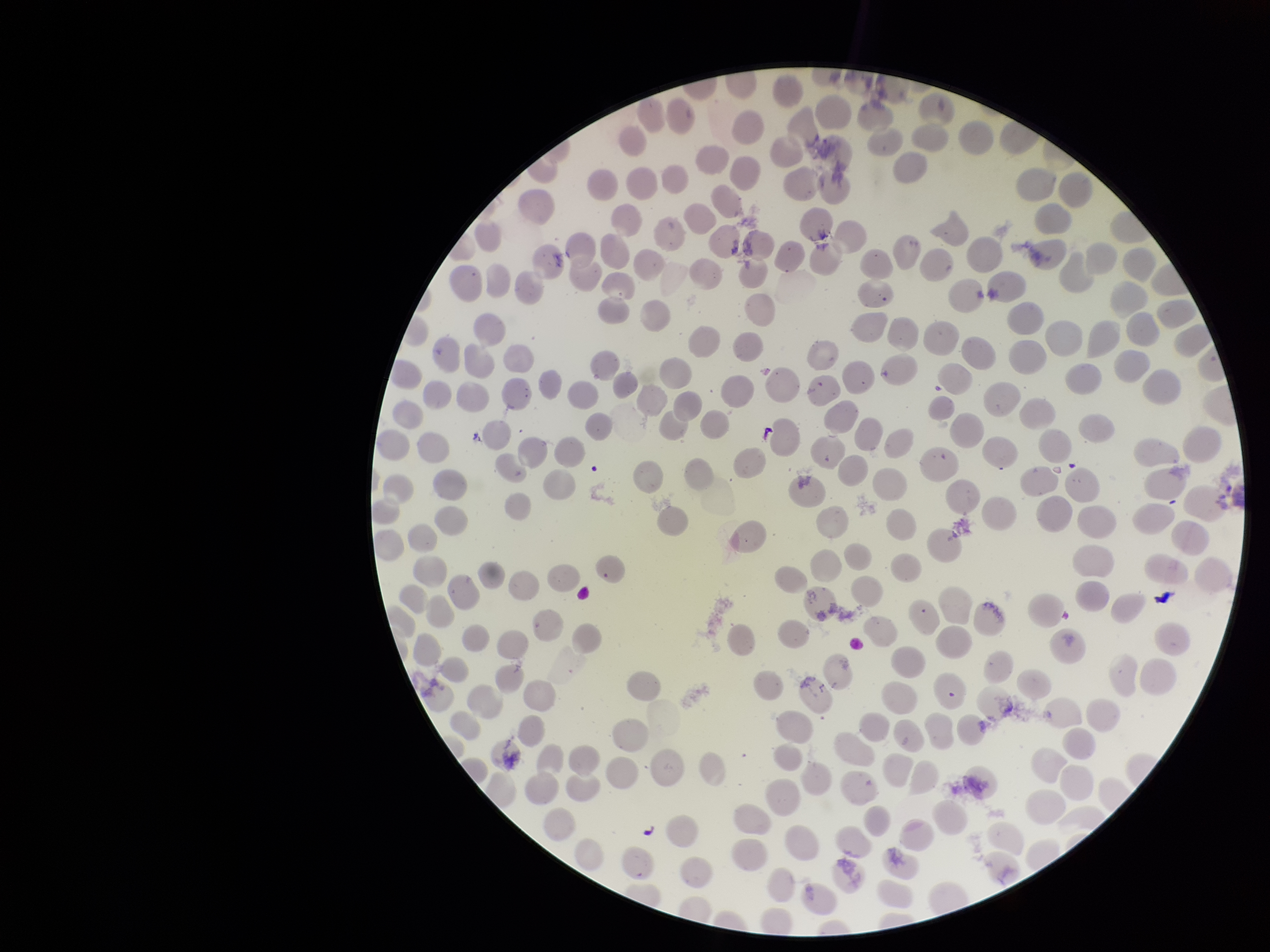

Summary:
  - Species reported for this patient: Plasmodium vivax
  - Field of view: single
  - Stain: Giemsa
  - Parasitized red blood cells: none seen
  - Image size: 1270×952 pixels
  - Preparation: thin
  - Red blood cell count: 205
  - Capture: smartphone photograph through the microscope eyepiece
  - Patient malaria status: positive
  - Parasitized red blood cell count: 0